Classify this cell by malaria status.
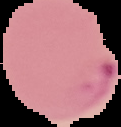
Parasitized.

Summary:
  - Image size: 121×127 pixels
  - Preparation: thin blood film
  - Image type: segmented cell region with the area outside set to black